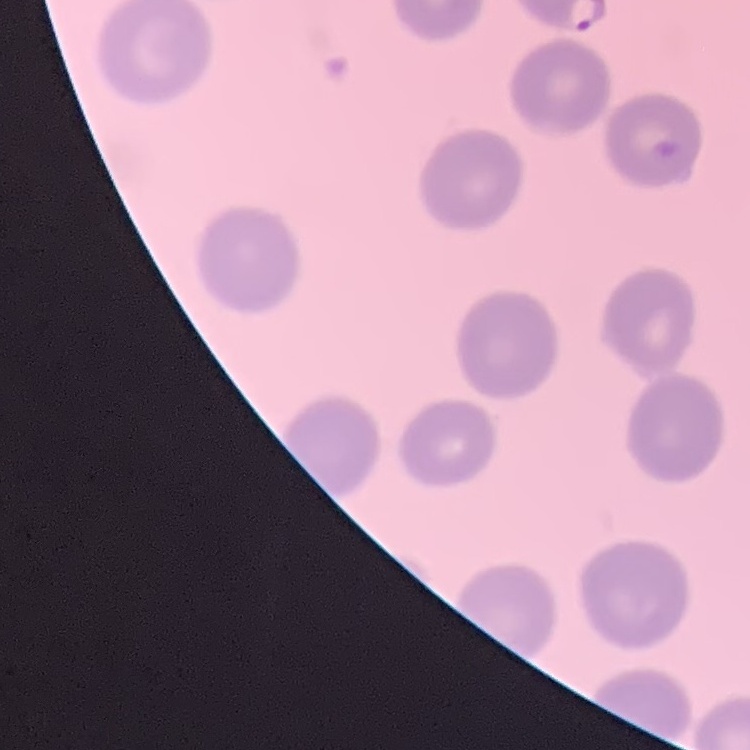
Summary:
  - Red blood cell morphology: no rouleaux formation
  - Stain: Field's or Giemsa
  - Preparation: thin peripheral smear
  - Image type: square crop of a larger photomicrograph